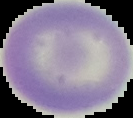

Result: no Plasmodium parasites detected. From a thin blood film. Segmented cell region on a black background. Image is 133×118 pixels.